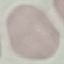

result = negative for malaria parasites
stain = Giemsa
image type = automatically extracted cell patch, resized to 64 × 64 pixels
preparation = thin smear
capture = smartphone through the microscope eyepiece